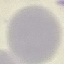

{
  "result": "no malaria parasites detected",
  "image_type": "automatically extracted cell patch, resized to 64 × 64 pixels",
  "preparation": "thin blood smear",
  "stain": "Giemsa",
  "capture": "smartphone camera at the microscope eyepiece"
}